Locate and identify every blood parasite.
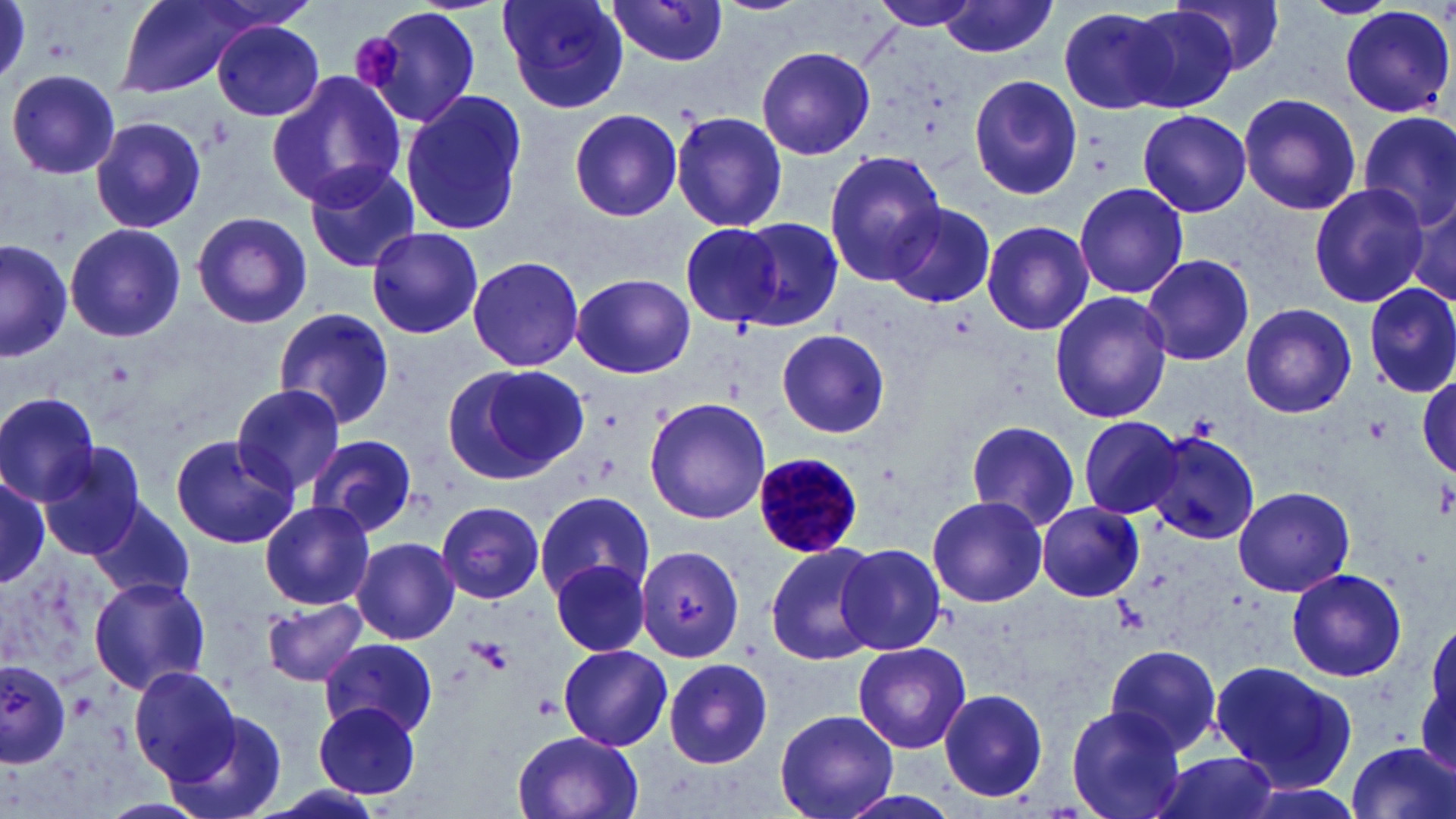
Approximate bounding boxes as named x1/y1/x2/y2 corners in pixels.
Plasmodium malariae-infected red blood cells: (x1=752, y1=452, x2=865, y2=558).
No Plasmodium falciparum, Plasmodium ovale, Plasmodium vivax, Babesia divergens, or Trypanosoma brucei observed.

Summary:
  - Uninfected red blood cell locations: (x1=112, y1=0, x2=262, y2=100), (x1=496, y1=0, x2=628, y2=113), (x1=866, y1=0, x2=991, y2=33), (x1=940, y1=0, x2=1058, y2=57), (x1=1174, y1=0, x2=1288, y2=75), (x1=1301, y1=0, x2=1399, y2=18), (x1=603, y1=1, x2=732, y2=68), (x1=352, y1=5, x2=486, y2=128), (x1=1057, y1=5, x2=1181, y2=114), (x1=1122, y1=6, x2=1241, y2=113), (x1=1340, y1=6, x2=1454, y2=118), (x1=210, y1=19, x2=326, y2=121), (x1=757, y1=44, x2=879, y2=159), (x1=7, y1=70, x2=120, y2=179), (x1=266, y1=71, x2=408, y2=207), (x1=968, y1=75, x2=1084, y2=200), (x1=397, y1=91, x2=527, y2=237), (x1=1238, y1=94, x2=1361, y2=215), (x1=569, y1=108, x2=686, y2=222), (x1=1138, y1=110, x2=1251, y2=217), (x1=671, y1=111, x2=788, y2=233), (x1=1356, y1=111, x2=1456, y2=235), (x1=90, y1=114, x2=207, y2=234), (x1=824, y1=149, x2=949, y2=286), (x1=304, y1=161, x2=421, y2=273), (x1=1073, y1=181, x2=1190, y2=299), (x1=1307, y1=184, x2=1429, y2=308), (x1=1409, y1=192, x2=1455, y2=305), (x1=885, y1=203, x2=995, y2=308), (x1=191, y1=211, x2=315, y2=329), (x1=727, y1=219, x2=842, y2=331), (x1=680, y1=220, x2=794, y2=332), (x1=981, y1=220, x2=1094, y2=337), (x1=64, y1=223, x2=186, y2=343), (x1=367, y1=228, x2=483, y2=339), (x1=0, y1=239, x2=72, y2=360), (x1=1141, y1=254, x2=1256, y2=367), (x1=467, y1=255, x2=585, y2=373), (x1=570, y1=273, x2=696, y2=379), (x1=1362, y1=282, x2=1456, y2=398), (x1=1049, y1=291, x2=1173, y2=425), (x1=1240, y1=303, x2=1357, y2=419), (x1=273, y1=308, x2=396, y2=430), (x1=775, y1=328, x2=890, y2=438), (x1=440, y1=363, x2=587, y2=487), (x1=1416, y1=373, x2=1455, y2=479), (x1=231, y1=383, x2=345, y2=493), (x1=0, y1=392, x2=101, y2=507), (x1=643, y1=396, x2=771, y2=525), (x1=1078, y1=414, x2=1183, y2=522), (x1=964, y1=418, x2=1082, y2=531), (x1=1144, y1=428, x2=1260, y2=544), (x1=1147, y1=430, x2=1261, y2=545), (x1=169, y1=433, x2=298, y2=549), (x1=308, y1=435, x2=419, y2=535), (x1=38, y1=442, x2=147, y2=560), (x1=0, y1=468, x2=47, y2=595), (x1=0, y1=474, x2=51, y2=587), (x1=1233, y1=485, x2=1355, y2=597), (x1=533, y1=493, x2=654, y2=604), (x1=926, y1=495, x2=1048, y2=607), (x1=90, y1=499, x2=195, y2=605), (x1=259, y1=501, x2=374, y2=609), (x1=433, y1=503, x2=549, y2=603), (x1=1035, y1=503, x2=1145, y2=602), (x1=351, y1=536, x2=461, y2=644), (x1=764, y1=542, x2=882, y2=668), (x1=834, y1=543, x2=948, y2=657), (x1=635, y1=544, x2=746, y2=663), (x1=550, y1=559, x2=651, y2=658), (x1=1285, y1=568, x2=1409, y2=682), (x1=89, y1=576, x2=213, y2=694), (x1=261, y1=594, x2=368, y2=688), (x1=321, y1=638, x2=438, y2=738), (x1=851, y1=641, x2=973, y2=754), (x1=557, y1=644, x2=673, y2=752), (x1=1100, y1=646, x2=1226, y2=753), (x1=661, y1=655, x2=776, y2=769), (x1=0, y1=660, x2=74, y2=766), (x1=1211, y1=660, x2=1358, y2=792), (x1=130, y1=666, x2=243, y2=783), (x1=938, y1=687, x2=1049, y2=804), (x1=314, y1=702, x2=421, y2=801), (x1=1066, y1=705, x2=1187, y2=819), (x1=164, y1=708, x2=289, y2=819), (x1=775, y1=708, x2=898, y2=819), (x1=510, y1=730, x2=645, y2=819), (x1=1346, y1=742, x2=1456, y2=819), (x1=1151, y1=752, x2=1284, y2=819), (x1=249, y1=779, x2=391, y2=819), (x1=832, y1=790, x2=968, y2=819)
  - Platelet locations: (x1=349, y1=32, x2=403, y2=91), (x1=1364, y1=417, x2=1393, y2=445), (x1=1436, y1=478, x2=1456, y2=517), (x1=471, y1=638, x2=515, y2=676), (x1=534, y1=694, x2=562, y2=720)
  - Slide-level diagnosis: Plasmodium malariae
  - Preparation: thin blood film
  - Magnification: 1000x
  - Image size: 1456×819 pixels
  - Stain: May-Grünwald-Giemsa
  - Field of view: single
  - Modality: optical microscopy